Give the extent of all uninfected red blood cells.
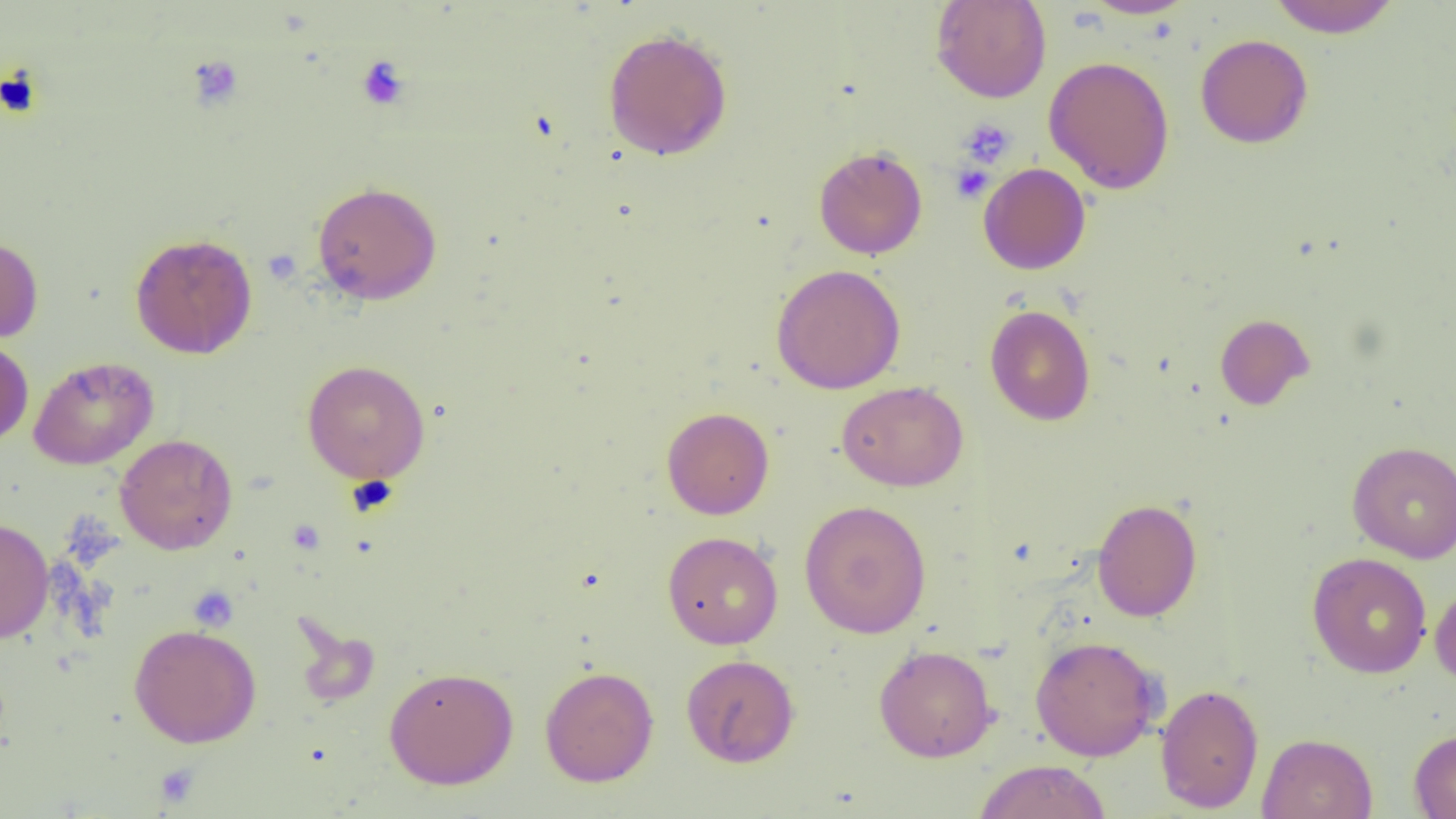

Approximate bounding boxes as [x1, y1, x2, y2] in pixels.
Uninfected red blood cells: [930, 0, 1052, 103], [1080, 0, 1196, 19], [1266, 0, 1402, 37], [602, 27, 733, 161], [1195, 33, 1314, 149], [1043, 56, 1176, 194], [813, 145, 928, 260], [978, 162, 1091, 275], [312, 181, 442, 304], [130, 232, 258, 359], [0, 236, 43, 344], [772, 263, 906, 394], [985, 304, 1096, 426], [1214, 313, 1314, 411], [0, 337, 34, 447], [28, 356, 158, 469], [302, 359, 430, 484], [837, 380, 969, 491], [661, 407, 774, 519], [115, 433, 238, 554], [1347, 440, 1456, 563], [1092, 498, 1203, 622], [799, 499, 932, 639], [0, 517, 54, 645], [662, 531, 783, 649], [1307, 552, 1432, 678], [1430, 578, 1456, 689], [129, 623, 262, 747], [1030, 635, 1162, 761], [874, 644, 997, 762], [680, 654, 801, 767], [539, 665, 659, 787], [383, 666, 519, 790], [1154, 683, 1265, 813], [1409, 729, 1456, 818], [1257, 732, 1378, 819], [973, 759, 1112, 818].

slide_level_diagnosis: negative for blood parasites
image_size: 1456×819 pixels
magnification: 1000x
platelet_locations: 'approximate bounding boxes as [x1, y1, x2, y2] in pixels: [186, 54, 244, 111], [356, 56, 410, 111], [958, 117, 1016, 168], [951, 163, 993, 203], [188, 586, 238, 632], [154, 763, 200, 808]'
field_of_view: single
modality: optical microscopy
preparation: thin blood smear